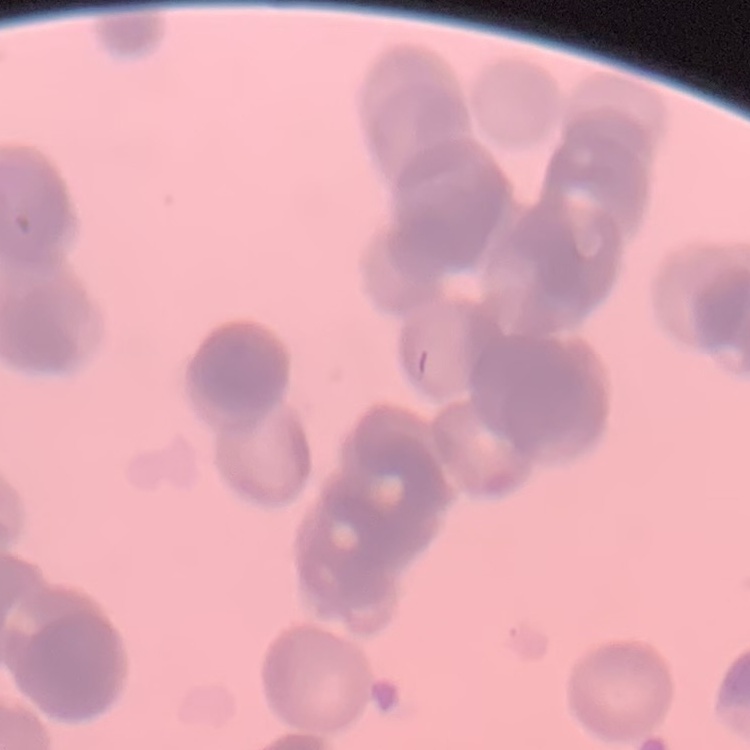
The red blood cells exhibit rouleaux formation. One tile cut from a larger photomicrograph. Field's or Giemsa stain. Thin blood film.